Give the extent of all uninfected red blood cells.
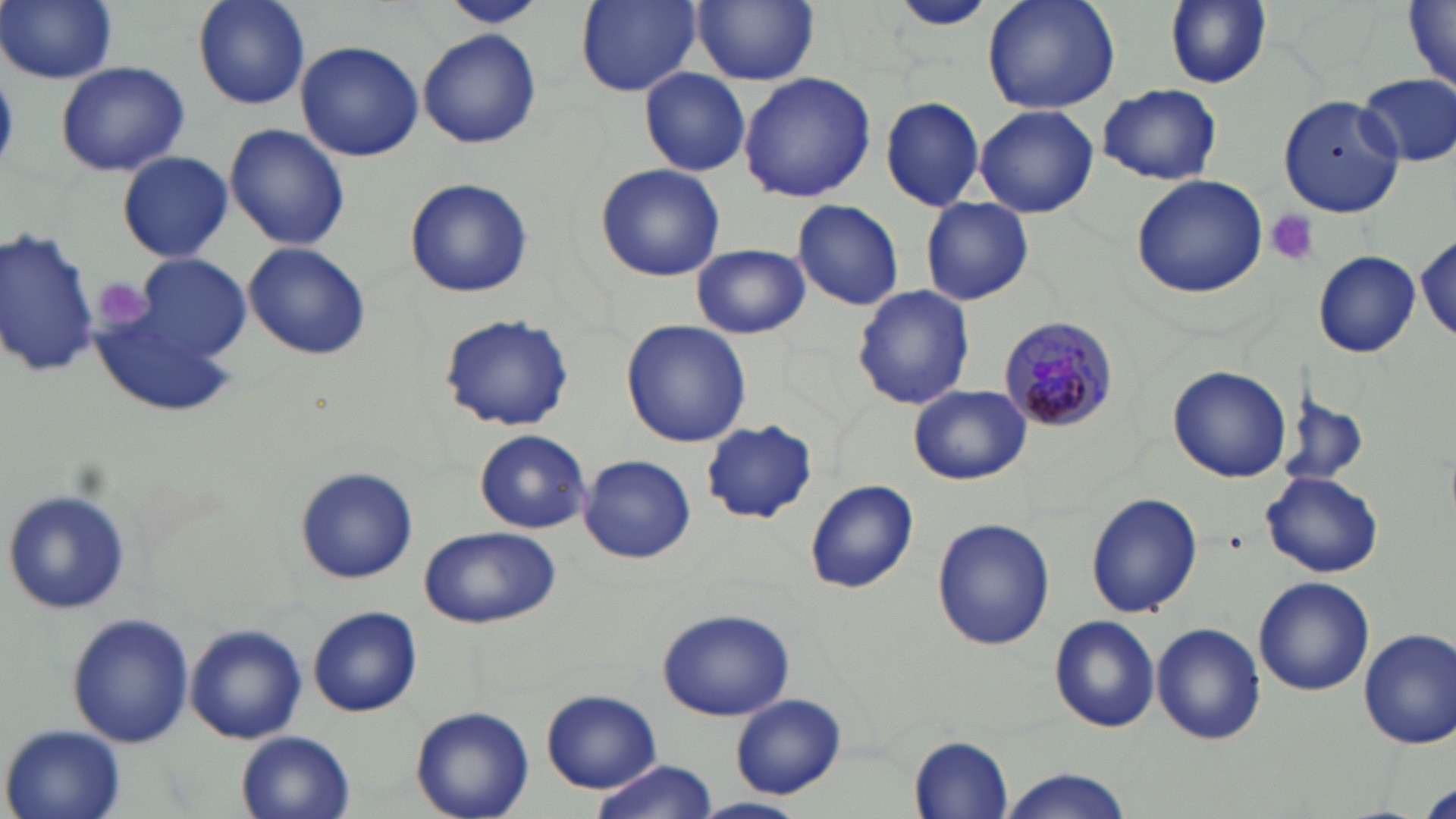

Approximate bounding boxes as (x1,y1)-(x2,y2) corner pairs in pixels.
Uninfected red blood cells: (0,0)-(118,85), (190,0)-(311,112), (439,0)-(548,27), (576,0)-(701,94), (692,0)-(818,85), (887,0)-(999,33), (982,0)-(1120,115), (1164,0)-(1272,88), (1403,1)-(1456,90), (417,27)-(542,151), (295,40)-(425,162), (55,62)-(189,176), (639,69)-(751,177), (738,72)-(877,202), (1355,74)-(1456,168), (1098,82)-(1224,185), (1278,96)-(1405,218), (880,97)-(985,210), (973,103)-(1100,218), (223,123)-(350,250), (117,151)-(232,262), (595,163)-(726,282), (1131,173)-(1270,298), (403,178)-(533,298), (921,197)-(1032,306), (792,199)-(904,310), (0,225)-(99,380), (1415,230)-(1455,341), (243,242)-(370,360), (692,243)-(810,339), (1315,252)-(1420,356), (136,254)-(251,359), (852,285)-(976,410), (91,310)-(237,418), (437,315)-(574,431), (622,319)-(751,448), (1169,364)-(1293,483), (909,385)-(1031,485), (1273,387)-(1372,491), (701,420)-(817,523), (475,430)-(591,534), (580,455)-(696,564), (294,465)-(417,583), (1261,469)-(1384,579), (806,480)-(918,593), (3,489)-(133,616), (1085,494)-(1203,619), (931,517)-(1056,651), (420,526)-(559,629), (1253,576)-(1374,696), (306,607)-(423,717), (654,607)-(796,719), (67,612)-(193,750), (1049,617)-(1159,730), (185,623)-(308,745), (1151,623)-(1264,745), (1359,627)-(1455,750), (539,687)-(665,795), (732,695)-(845,799), (410,705)-(534,819), (0,721)-(128,819), (236,732)-(354,819), (909,735)-(1012,815), (588,761)-(719,819), (998,769)-(1135,819), (1419,781)-(1456,819), (695,796)-(807,819).

Platelet locations: (1266,210)-(1318,268), (91,277)-(158,337). Plasmodium malariae-infected red blood cell locations: (1000,315)-(1119,437). Slide-level diagnosis: Plasmodium malariae. Captured at 1000x magnification. Thin blood film. Image is 1456×819 pixels. May-Grünwald-Giemsa-stained preparation. One field of a larger specimen. Light microscopy.